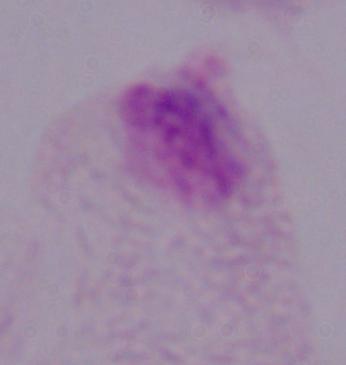

1000x magnification. A trichomonad is seen. Micrograph.